Point out each Plasmodium parasite.
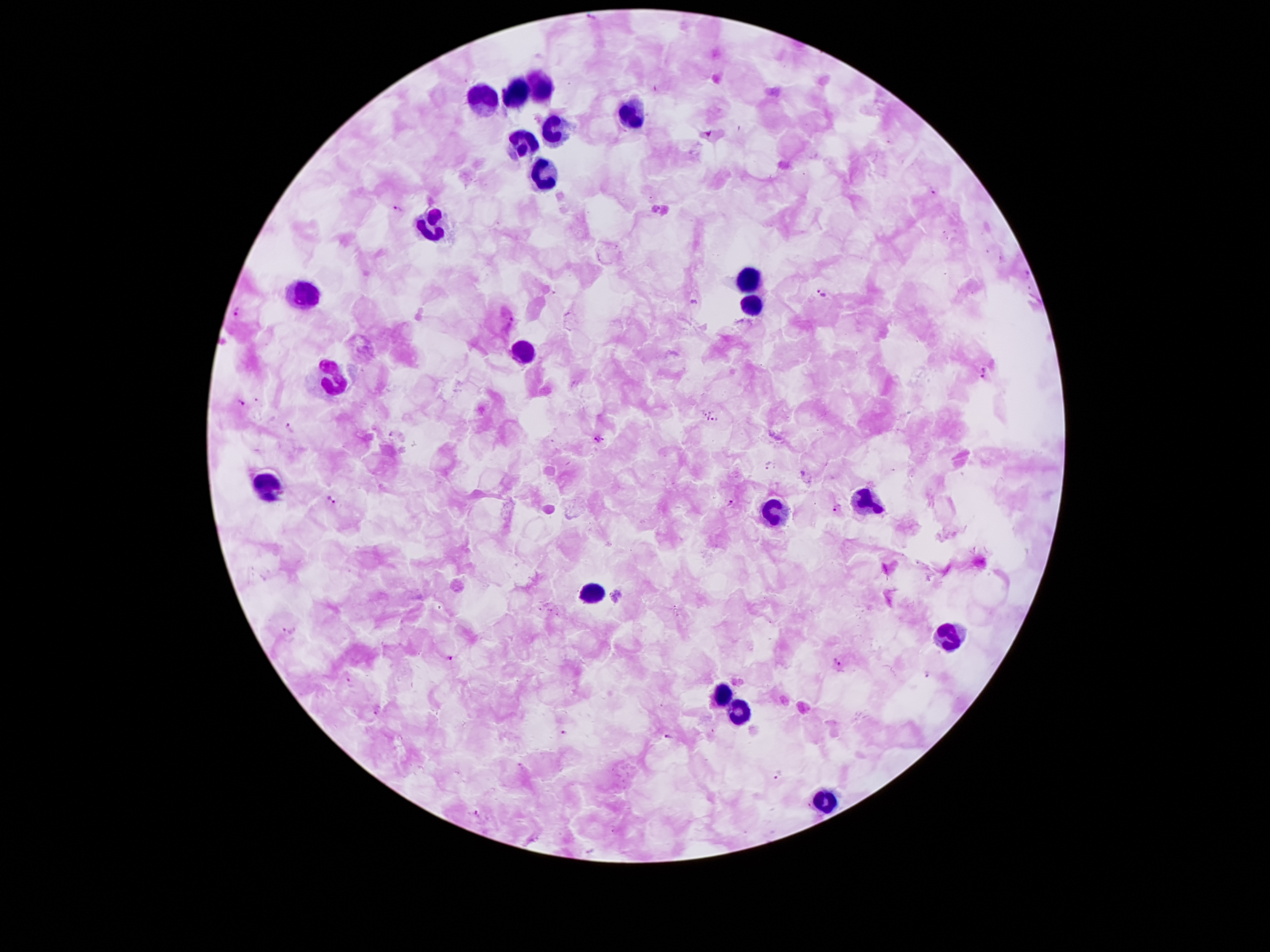

Approximate centers as (x, y) in pixels.
Plasmodium parasites: (934, 192), (398, 211), (824, 293), (236, 312), (985, 372), (241, 403), (704, 412), (712, 412), (708, 419), (714, 421), (288, 426), (595, 439), (605, 441), (769, 465), (330, 500), (731, 503), (838, 508), (289, 630), (449, 658), (835, 660), (928, 675), (350, 683), (377, 712), (563, 733), (668, 736), (780, 777), (477, 813).

Summary:
  - Leukocyte locations: (543, 90), (516, 92), (478, 96), (633, 108), (549, 127), (522, 144), (539, 172), (432, 223), (751, 281), (306, 290), (749, 309), (526, 352), (333, 380), (268, 482), (866, 498), (770, 505), (593, 591), (950, 640), (721, 694), (738, 714), (824, 805)
  - Patient malaria status: positive for Plasmodium falciparum
  - Preparation: thick peripheral-blood smear
  - Magnification: 100x
  - Stain: Giemsa
  - Field of view: single
  - Image size: 1270×952 pixels
  - Capture: smartphone camera through the microscope eyepiece